Report the malaria status of this cell.
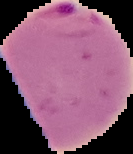
It is parasitized.

preparation = thin blood film
image size = 133×154 pixels
image type = segmented cell region with the area outside set to black